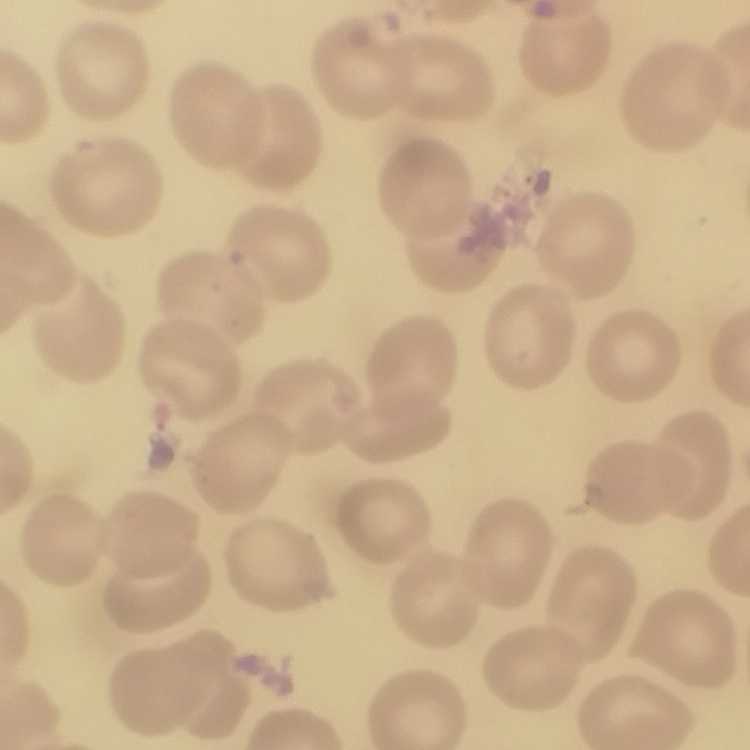
Summary:
  - Erythrocyte morphology: no rouleaux formation
  - Preparation: thin peripheral smear
  - Stain: Field's or Giemsa
  - Image type: one tile cut from a larger photomicrograph